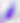

Toxoplasma gondii is shown. 400x magnification. Micrograph.